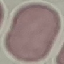
Summary:
  - Malaria status: uninfected
  - Image type: automatically extracted cell patch, resized to 64 × 64 pixels
  - Capture: smartphone camera at the microscope eyepiece
  - Stain: Giemsa
  - Preparation: thin smear